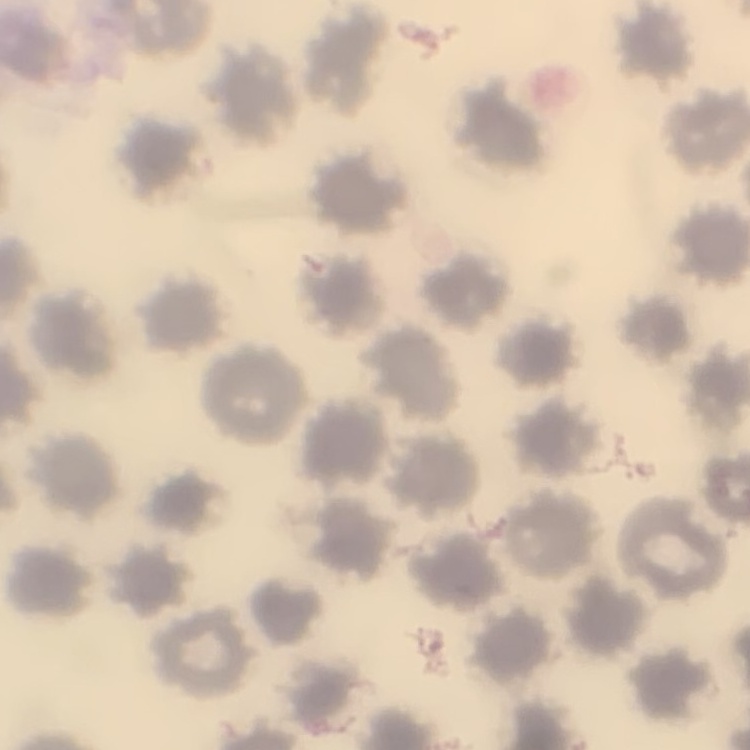 The erythrocytes show no rouleaux formation. Thin peripheral smear. Field's or Giemsa stain. Square crop of a larger photomicrograph.